Report the malaria status of this cell.
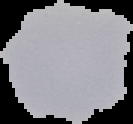
Uninfected.

Cell region segmented out of the field of view; the surrounding area is masked to black. From a thin blood smear. Image is 133×124 pixels.